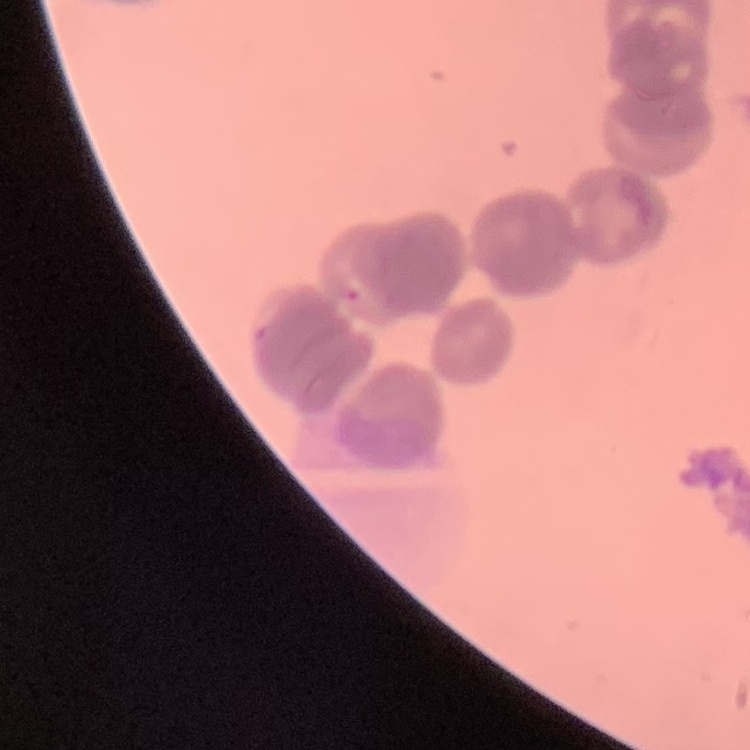

Summary:
  - Red blood cell morphology: rouleaux formation
  - Preparation: thin blood smear
  - Stain: Field's or Giemsa
  - Image type: one tile cut from a larger photomicrograph